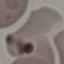
Malaria status: uninfected. Photographed with a smartphone camera at the microscope eyepiece. Thin blood film. Automatically extracted cell patch, resized to 64 × 64 pixels. Giemsa-stained preparation.